Report the malaria status of this cell.
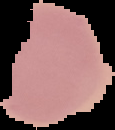

Uninfected.

Summary:
  - Image size: 115×130 pixels
  - Preparation: thin blood film
  - Image type: cell region segmented out of the field of view; surrounding area masked to black